Report the malaria status of this cell.
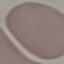
It is uninfected.

Summary:
  - Capture: smartphone camera at the microscope eyepiece
  - Preparation: thin blood smear
  - Stain: Giemsa
  - Image type: cell patch, automatically extracted from a larger field of view and resized to 64 × 64 pixels